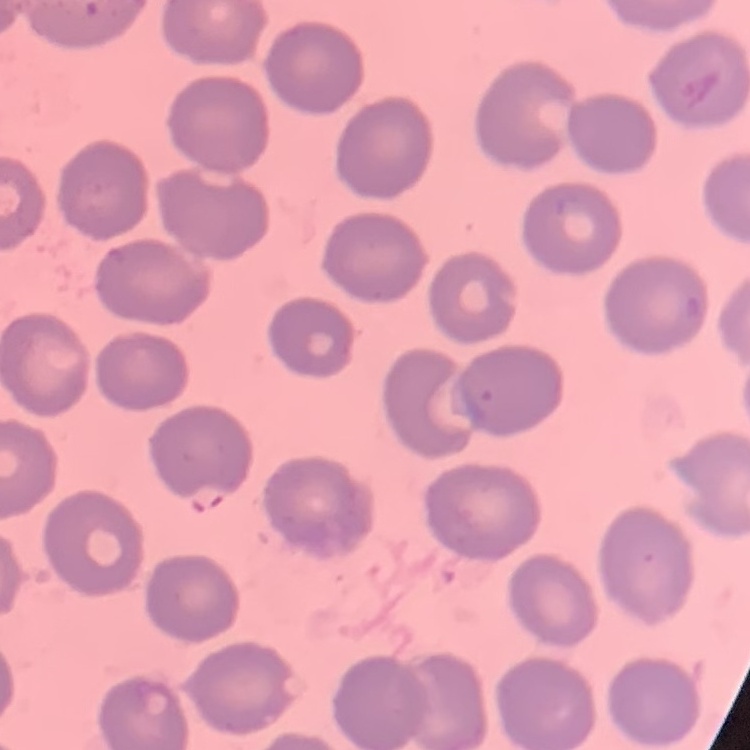
red_blood_cell_morphology: no rouleaux formation
stain: Field's or Giemsa
preparation: thin peripheral smear
image_type: square crop of a larger photomicrograph